Assess the morphology of the red blood cells.
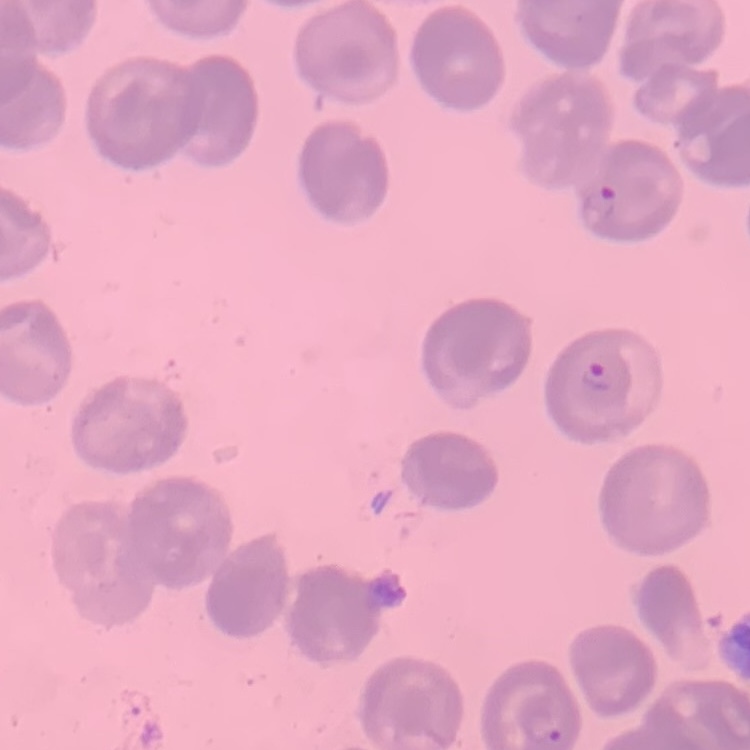
They show no rouleaux formation.

Field's or Giemsa stain. One tile cut from a larger photomicrograph. Thin blood smear.